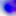
Captured at 400x magnification. Toxoplasma gondii is seen. Photomicrograph.